State which parasite is depicted.
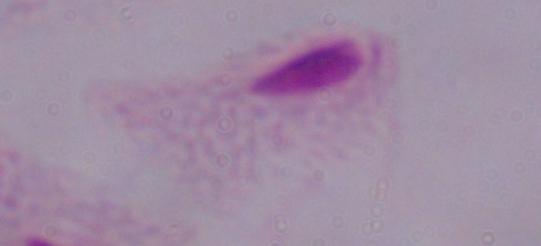
This is a trichomonad.

Summary:
  - Modality: micrograph
  - Magnification: 1000x